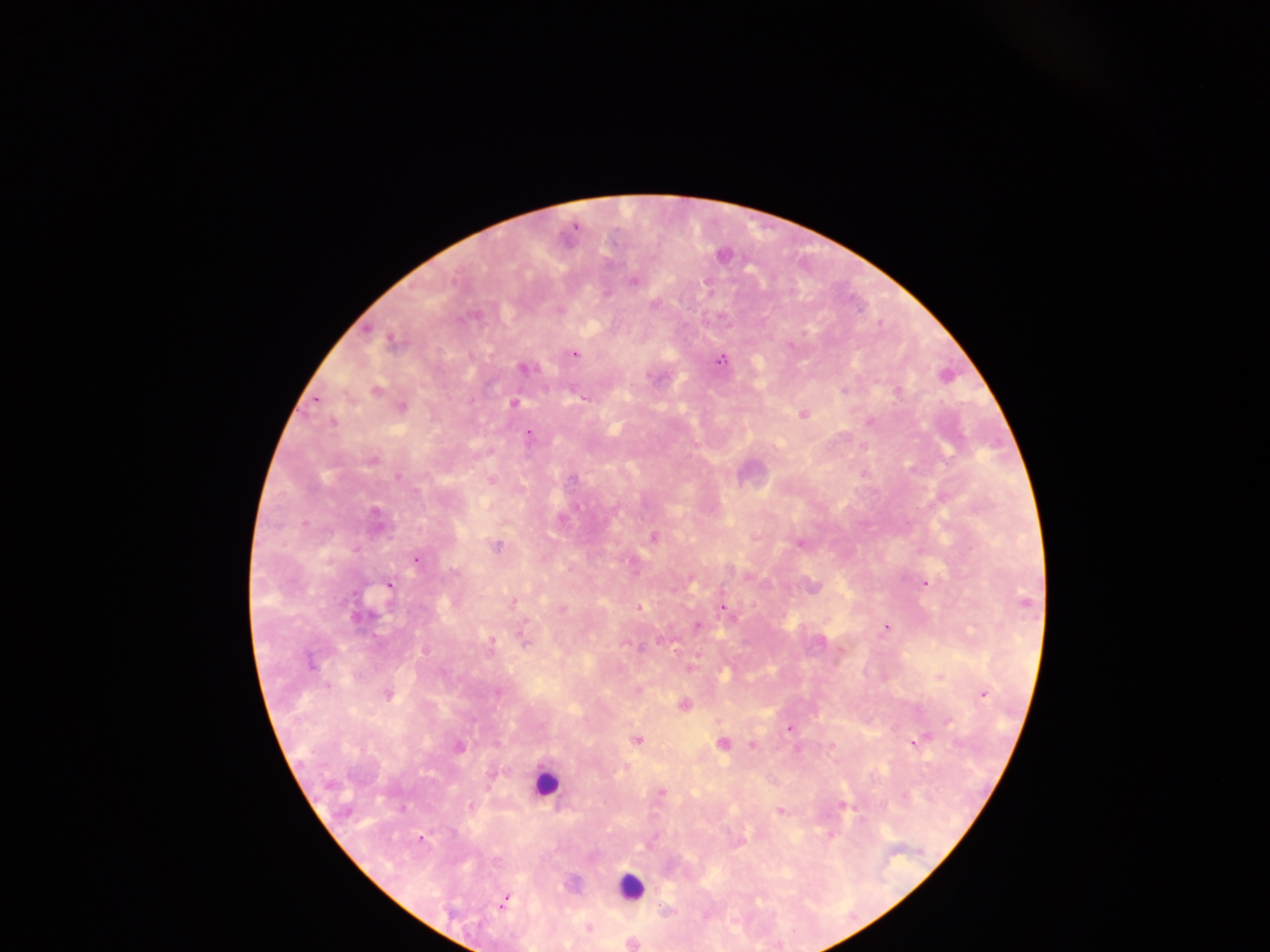 Approximate centers as [x, y] in pixels. Leukocyte locations: [545, 784], [629, 886]. Malaria parasite locations: [722, 256], [633, 280], [606, 294], [654, 304], [559, 310], [391, 342], [574, 354], [721, 360], [524, 368], [376, 390], [843, 391], [897, 391], [583, 399], [316, 400], [513, 403], [402, 406], [804, 414], [332, 421], [871, 421], [528, 434], [372, 460], [398, 476], [572, 479], [577, 506], [654, 537], [798, 544], [496, 546], [416, 561], [633, 563], [455, 572], [925, 583], [389, 585], [1026, 600], [513, 602], [640, 607], [723, 607], [561, 609], [358, 618], [697, 626], [887, 627], [525, 641], [820, 641], [491, 643], [639, 648], [424, 651], [310, 663], [691, 666], [329, 686], [637, 691], [498, 692], [983, 694], [387, 695], [683, 705], [948, 721], [789, 728], [923, 738], [637, 739], [913, 742], [723, 744], [752, 745], [459, 746], [662, 793], [905, 796], [470, 805], [842, 805], [402, 808], [779, 811], [420, 839], [505, 900], [665, 909], [589, 928], [631, 944]. Single field of view. Sample from Ghana. Photographed through a microscope with a mobile-phone camera. Image is 1270×952 pixels. Thick blood smear.